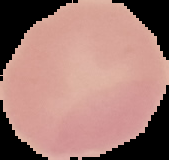
Cell region segmented out of the field of view; the surrounding area is masked to black. Result: no malaria parasites detected. From a thin blood smear. Image is 169×160 pixels.